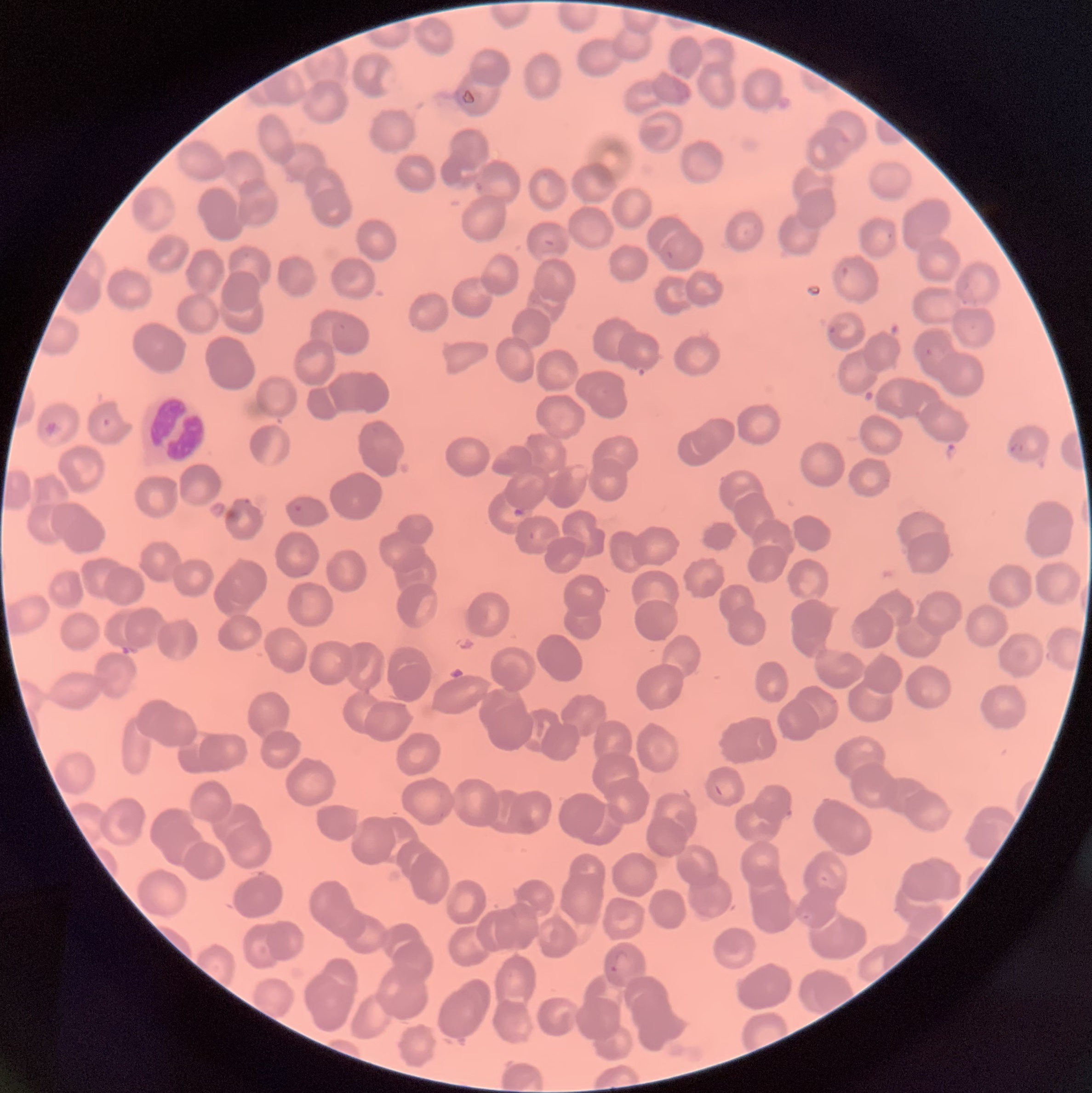
Summary:
  - Coordinate format: approximate bounding boxes as named x1/y1/x2/y2 corners in pixels
  - Plasmodium parasites too small for a box (approximate object centers, named x/y in pixels): (x=964, y=302)
  - Plasmodium parasite locations: (x1=674, y1=65, x2=684, y2=75), (x1=838, y1=130, x2=851, y2=144), (x1=743, y1=229, x2=750, y2=237), (x1=887, y1=231, x2=893, y2=239), (x1=544, y1=238, x2=556, y2=247), (x1=665, y1=249, x2=675, y2=260), (x1=840, y1=266, x2=850, y2=277), (x1=829, y1=327, x2=837, y2=334), (x1=925, y1=348, x2=933, y2=355), (x1=101, y1=417, x2=112, y2=427), (x1=1009, y1=443, x2=1025, y2=452), (x1=242, y1=495, x2=252, y2=507), (x1=294, y1=503, x2=304, y2=513), (x1=528, y1=530, x2=535, y2=540), (x1=800, y1=911, x2=813, y2=923), (x1=609, y1=949, x2=632, y2=976)
  - White blood cell locations: (x1=145, y1=399, x2=207, y2=461)
  - Modality: optical microscopy
  - Preparation: thin blood film
  - Red blood cell morphology: rouleaux formation
  - Image size: 1092×1093 pixels